Assess for malaria.
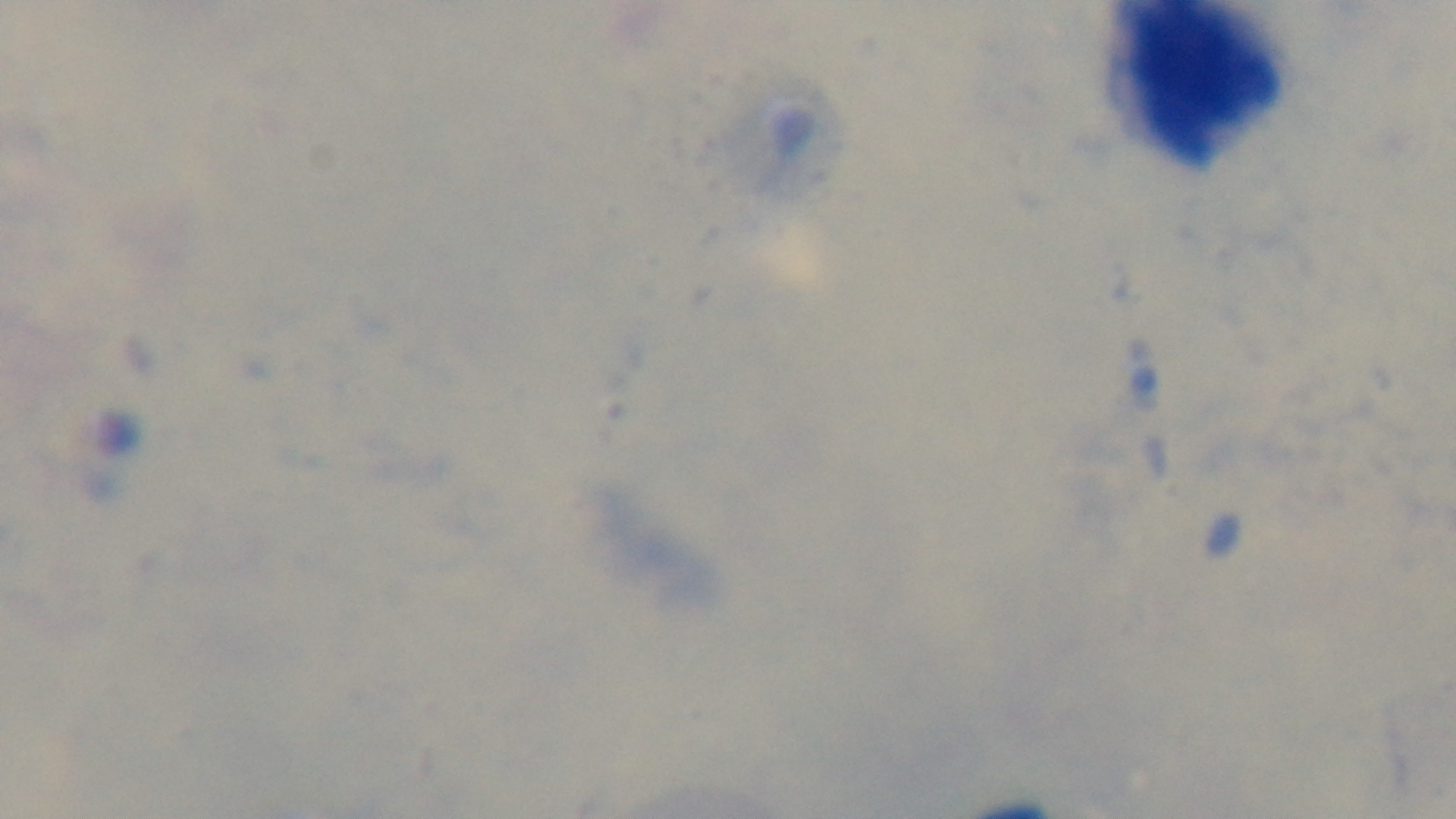
It is uninfected.

Summary:
  - Preparation: thick blood film
  - Capture: mounted 4K digital camera
  - Objective: 100x oil immersion
  - Modality: light microscopy
  - Field of view: single
  - Stain: Giemsa